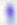

{
  "magnification": "400x",
  "modality": "photomicrograph",
  "identification": "Toxoplasma gondii"
}